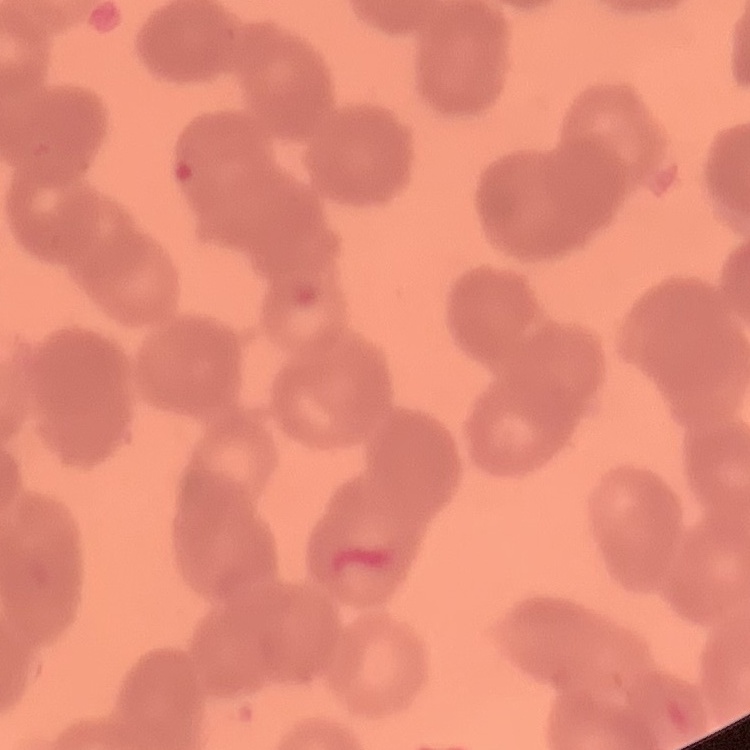

Summary:
  - Red blood cell morphology: rouleaux formation
  - Stain: Field's or Giemsa
  - Preparation: thin blood smear
  - Image type: square crop of a larger photomicrograph